Locate and identify every blood parasite.
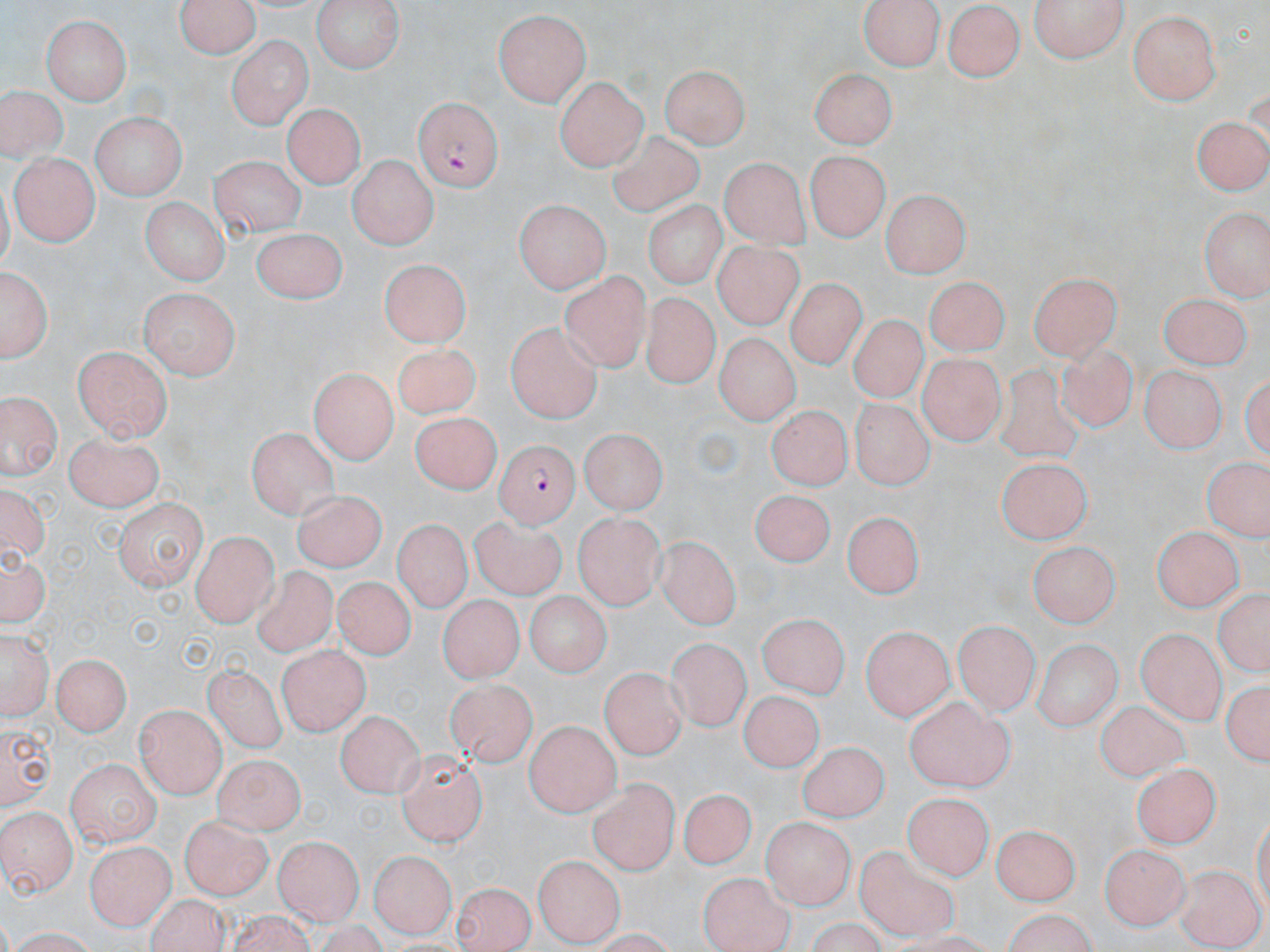

Approximate bounding boxes as [x1, y1, x2, y2] in pixels.
Plasmodium falciparum-infected red blood cells: [415, 96, 503, 192], [496, 442, 578, 527].
No Plasmodium ovale, Plasmodium malariae, Plasmodium vivax, Babesia divergens, or Trypanosoma brucei observed.

slide-level diagnosis = Plasmodium falciparum
preparation = thin blood smear
field of view = one of a larger specimen
magnification = 1000x
image size = 1270×952 pixels
modality = optical microscopy
stain = May-Grünwald-Giemsa
uninfected red blood cell locations = approximate bounding boxes as [x1, y1, x2, y2] in pixels: [174, 0, 262, 58], [309, 0, 403, 73], [861, 0, 940, 71], [1028, 0, 1131, 62], [944, 2, 1025, 81], [1127, 7, 1224, 105], [492, 8, 594, 107], [43, 12, 131, 104], [228, 35, 313, 129], [662, 63, 748, 149], [811, 66, 894, 149], [554, 73, 650, 169], [1, 84, 64, 164], [279, 103, 366, 189], [1196, 110, 1268, 196], [91, 112, 182, 203], [607, 129, 702, 216], [809, 149, 888, 242], [10, 152, 96, 248], [349, 154, 434, 249], [206, 155, 304, 235], [720, 158, 808, 249], [882, 191, 967, 279], [138, 197, 228, 286], [515, 197, 611, 293], [642, 201, 723, 293], [1200, 207, 1270, 296], [254, 227, 344, 305], [716, 238, 806, 332], [378, 260, 467, 348], [0, 263, 54, 362], [1028, 267, 1124, 358], [560, 269, 651, 374], [924, 277, 1007, 355], [788, 279, 867, 371], [139, 286, 239, 378], [1151, 289, 1256, 375], [637, 290, 721, 388], [850, 316, 935, 401], [508, 322, 603, 425], [714, 332, 798, 428], [1056, 344, 1136, 434], [75, 346, 171, 442], [394, 347, 480, 419], [916, 353, 1002, 445], [999, 361, 1080, 463], [1141, 363, 1224, 447], [305, 369, 393, 463], [2, 387, 60, 482], [852, 399, 933, 488], [768, 407, 849, 489], [409, 413, 504, 495], [245, 424, 335, 516], [580, 429, 665, 516], [66, 431, 165, 509], [1203, 452, 1270, 550], [999, 456, 1095, 541], [752, 488, 837, 564], [296, 489, 385, 574], [110, 499, 207, 587], [840, 512, 922, 600], [575, 514, 664, 608], [471, 517, 568, 597], [391, 519, 470, 618], [1153, 521, 1243, 609], [194, 532, 274, 627], [657, 533, 740, 630], [1026, 541, 1121, 628], [1, 545, 49, 628], [252, 565, 336, 660], [332, 577, 416, 658], [1215, 585, 1266, 682], [523, 591, 613, 675], [437, 597, 522, 686], [757, 611, 848, 700], [954, 620, 1038, 715], [863, 624, 954, 722], [1140, 624, 1228, 717], [2, 628, 50, 721], [1031, 637, 1124, 730], [667, 638, 748, 730], [277, 640, 365, 734], [51, 651, 131, 736], [205, 660, 284, 753], [604, 661, 688, 758], [1221, 675, 1269, 771], [447, 678, 538, 766], [737, 696, 824, 772], [906, 697, 1013, 793], [1094, 701, 1192, 781], [137, 706, 225, 795], [333, 714, 427, 797], [0, 717, 54, 809], [526, 719, 618, 818], [798, 740, 889, 820], [396, 751, 485, 849], [65, 756, 158, 844], [214, 757, 306, 841], [1134, 764, 1234, 850], [590, 778, 677, 874], [679, 791, 755, 872], [904, 793, 992, 880], [0, 804, 77, 897], [178, 815, 269, 898], [764, 815, 853, 911], [997, 823, 1076, 908], [273, 834, 362, 926], [1100, 840, 1191, 927], [85, 841, 175, 930], [853, 846, 962, 940], [368, 847, 454, 935], [535, 853, 622, 947], [1174, 867, 1263, 948], [700, 871, 794, 952], [450, 885, 537, 952]